Outline every leukocyte.
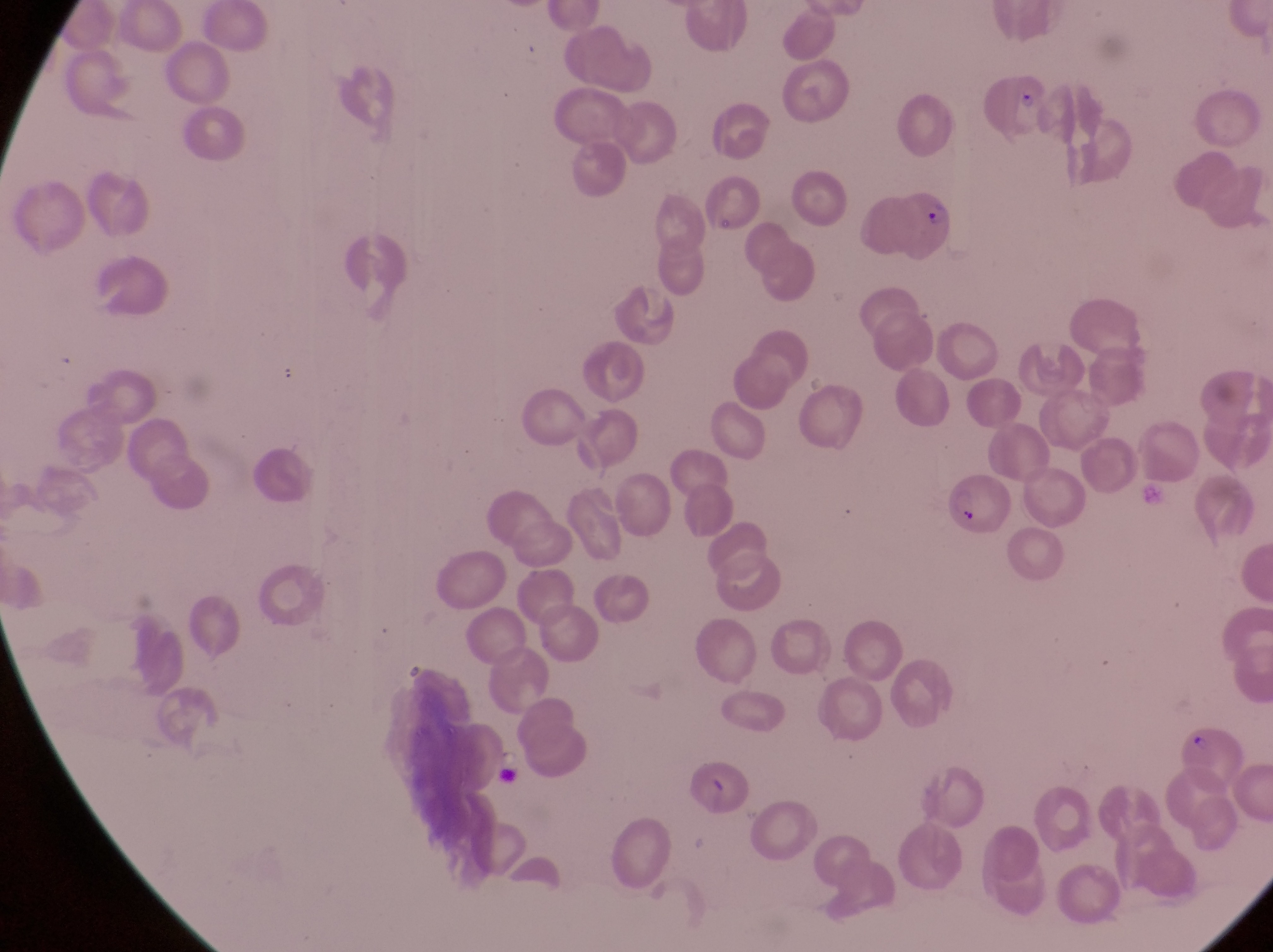

No leukocytes observed.

magnification = 1000x
field of view = single
parasitised red blood cell locations = approximate bounding boxes as {left, top, right, bottom} in pixels: {978, 72, 1053, 144}, {866, 183, 958, 271}
capture = smartphone photograph through the eyepiece of an Olympus CX-23 microscope
preparation = thin blood film
image size = 1273×952 pixels
country = Uganda